Report the malaria status.
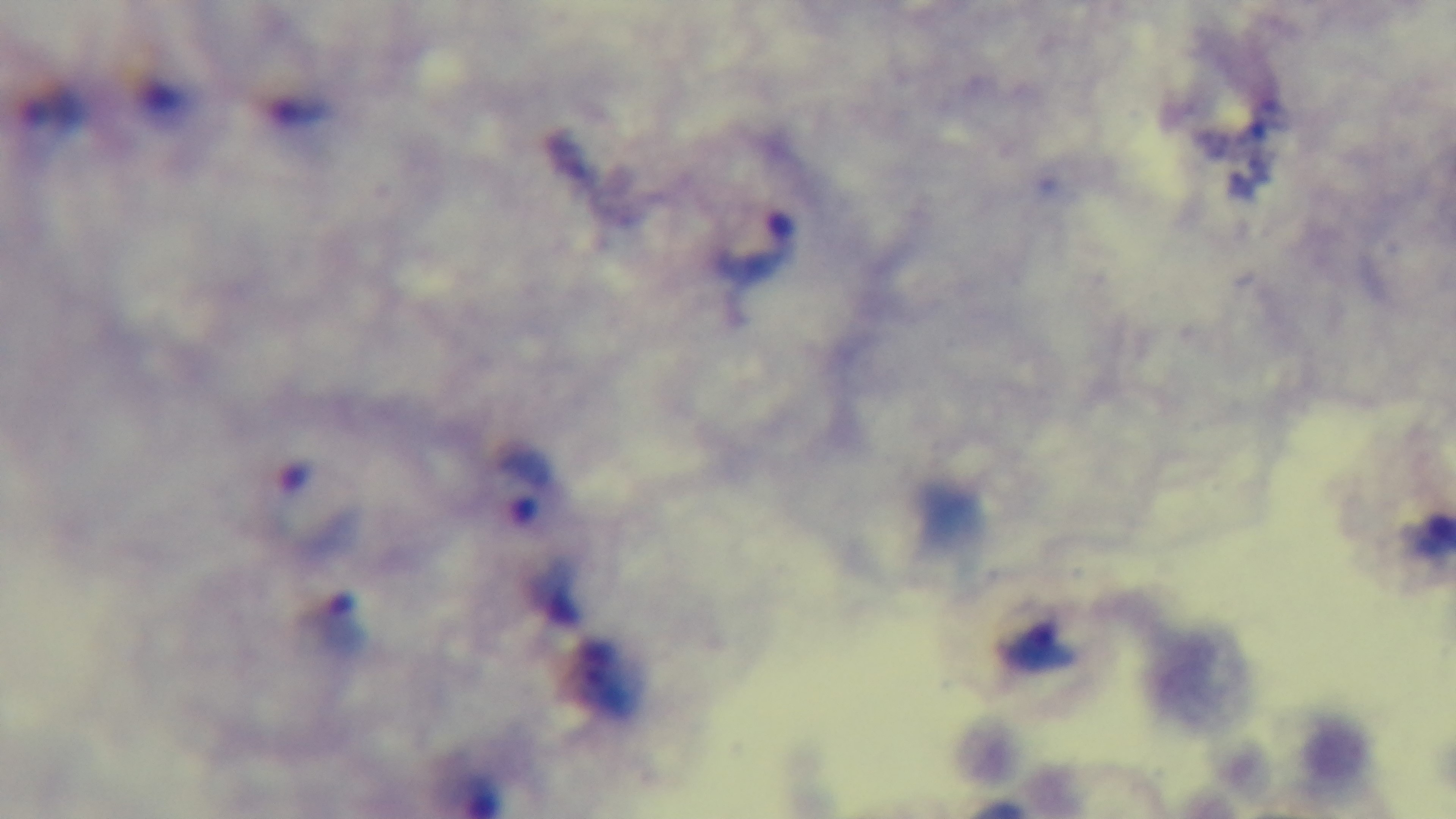
It is infected.

preparation: thick blood film
modality: light microscopy
capture: mounted 4K digital camera
stain: Giemsa
objective: 100x oil immersion
field_of_view: single